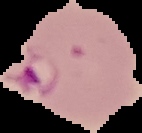
{
  "image_size": "142×133 pixels",
  "malaria_status": "parasitized",
  "preparation": "thin blood smear",
  "image_type": "cell region segmented out of the field of view; surrounding area masked to black"
}